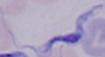
magnification = 1000x
identification = trypanosome
modality = micrograph